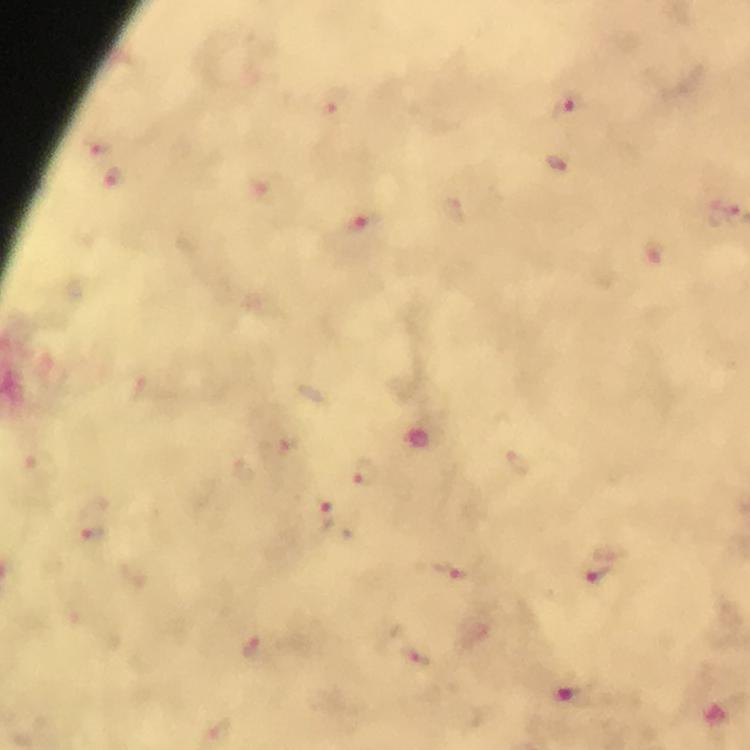

Approximate centers as [x, y] in pixels.
Summary:
  - Plasmodium parasite locations: [337, 102], [567, 107], [102, 146], [114, 176], [724, 215], [363, 225], [367, 474], [327, 517], [93, 535], [452, 572], [598, 574], [252, 648], [421, 657]
  - Stain: Giemsa
  - Magnification: 100x
  - Cropped from: one field of view
  - Preparation: thick smear
  - Context: from a diagnostic examination for malaria
  - Capture: smartphone photograph through a microscope
  - Immersion oil: applied
  - Image size: 750×750 pixels